Assess this cell for malaria.
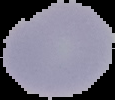

Uninfected.

image_size: 115×100 pixels
image_type: cell region segmented out of the field of view; surrounding area masked to black
preparation: thin blood film